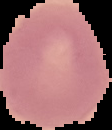

result = negative for Plasmodium parasites
image type = cell region segmented out of the field of view; surrounding area masked to black
image size = 112×130 pixels
preparation = thin blood film